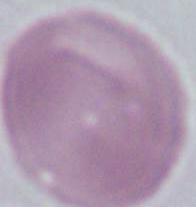
Summary:
  - Modality: micrograph
  - Identification: erythrocyte
  - Magnification: 1000x